Name the parasite shown.
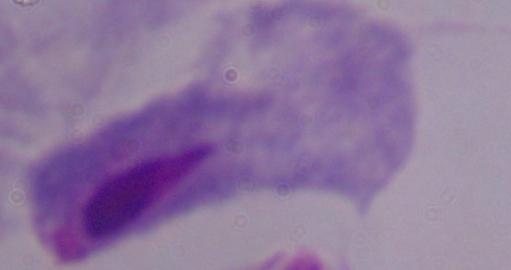

This is a trichomonad.

Summary:
  - Modality: photomicrograph
  - Magnification: 1000x